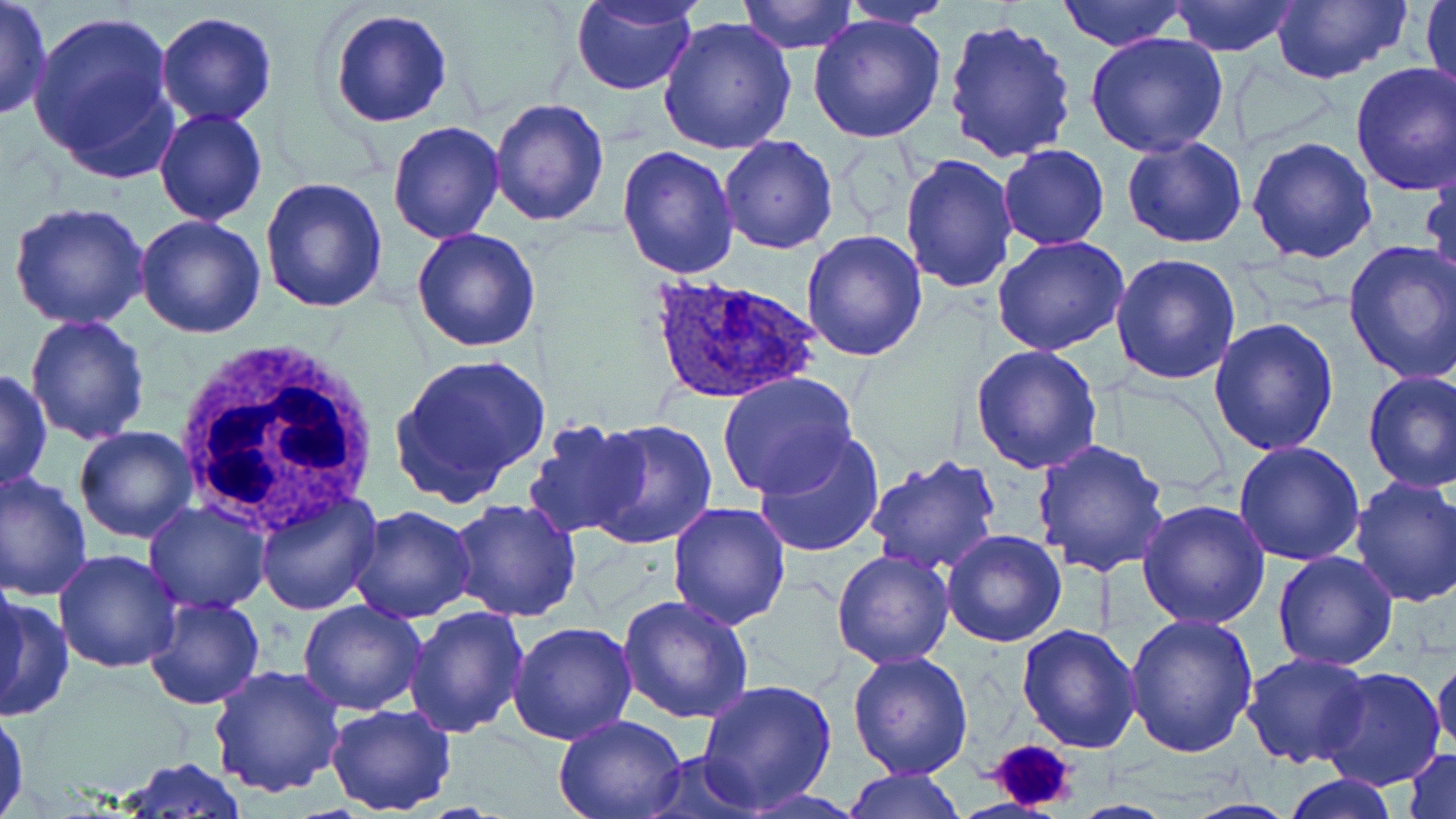
Approximate bounding boxes as [x1, y1, x2, y2] in pixels. Uninfected red blood cell locations: [0, 0, 50, 121], [1055, 0, 1185, 51], [1269, 0, 1409, 84], [1422, 0, 1456, 101], [571, 1, 697, 96], [737, 1, 858, 52], [841, 1, 950, 28], [1168, 1, 1303, 56], [25, 8, 178, 172], [330, 9, 453, 127], [806, 10, 949, 143], [155, 12, 277, 126], [657, 17, 798, 157], [941, 18, 1077, 164], [1084, 33, 1229, 157], [1350, 60, 1455, 196], [489, 96, 610, 227], [153, 108, 268, 226], [388, 121, 504, 244], [718, 135, 840, 256], [1120, 135, 1248, 248], [1247, 135, 1379, 263], [998, 144, 1108, 250], [617, 145, 740, 281], [899, 153, 1017, 291], [1423, 159, 1456, 287], [259, 175, 389, 313], [7, 202, 152, 331], [135, 214, 267, 337], [412, 227, 543, 352], [800, 229, 928, 360], [991, 235, 1131, 356], [1341, 238, 1456, 384], [1112, 254, 1241, 387], [24, 314, 151, 446], [1208, 316, 1341, 456], [970, 345, 1103, 474], [392, 354, 551, 503], [0, 369, 51, 494], [716, 372, 861, 499], [1363, 372, 1456, 494], [524, 416, 651, 539], [585, 417, 718, 549], [74, 426, 198, 545], [749, 428, 888, 559], [1032, 438, 1171, 579], [1233, 442, 1366, 567], [865, 456, 1002, 574], [1, 472, 92, 605], [1347, 476, 1456, 610], [254, 492, 379, 615], [143, 499, 272, 613], [449, 499, 582, 623], [1137, 499, 1271, 629], [666, 501, 792, 628], [347, 507, 476, 624], [941, 529, 1066, 648], [831, 549, 956, 670], [53, 550, 183, 674], [1272, 551, 1400, 672], [0, 575, 25, 705], [143, 594, 267, 711], [616, 594, 753, 723], [0, 596, 73, 722], [297, 600, 425, 717], [403, 605, 531, 738], [1125, 613, 1260, 761], [507, 622, 638, 745], [1016, 622, 1144, 753], [846, 650, 974, 779], [1240, 653, 1372, 769], [1433, 654, 1456, 757], [211, 663, 345, 797], [1316, 666, 1446, 791], [696, 677, 840, 812], [325, 704, 458, 816], [0, 708, 29, 817], [553, 714, 688, 819], [1405, 747, 1455, 819], [642, 750, 761, 819], [115, 758, 247, 816], [840, 767, 965, 819], [1280, 773, 1400, 819], [1176, 796, 1299, 818]. Platelet locations: [985, 737, 1081, 814]. White blood cell locations: [172, 342, 382, 536]. Plasmodium ovale-infected red blood cell locations: [649, 276, 823, 406]. Slide-level diagnosis: Plasmodium ovale. May-Grünwald-Giemsa stain. Single field of view. Optical microscopy. Thin blood smear. Captured at 1000x magnification. Image is 1456×819 pixels.